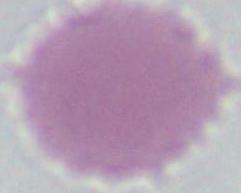
{
  "magnification": "1000x",
  "identification": "erythrocyte",
  "modality": "micrograph"
}